Comment on the morphology of the red blood cells.
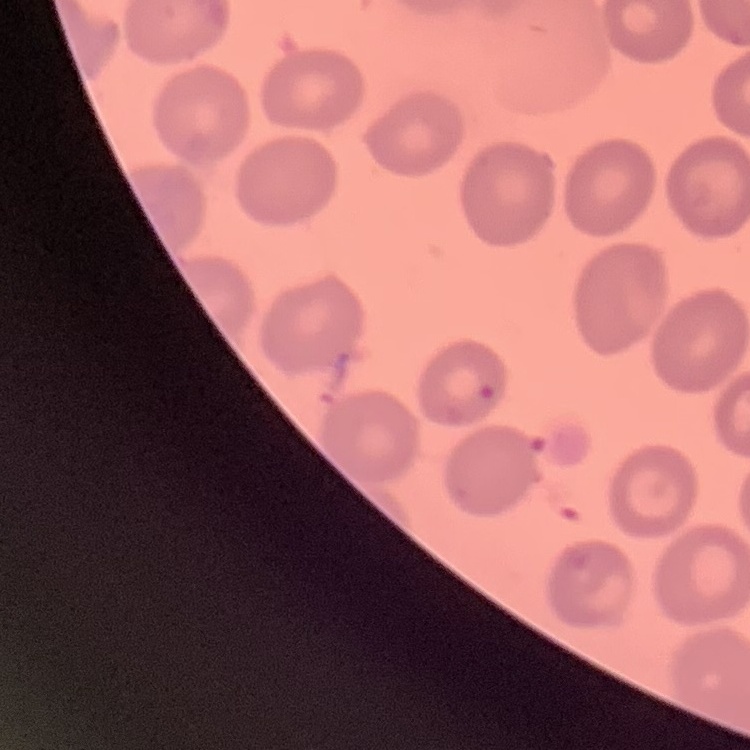
They show no rouleaux formation.

Summary:
  - Stain: Field's or Giemsa
  - Preparation: thin peripheral smear
  - Image type: one tile cut from a larger photomicrograph